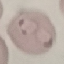 Result: malaria parasites detected. Giemsa stain. Photographed with a smartphone camera at the microscope eyepiece. Thin blood smear. Cell patch, automatically extracted from a larger field of view and resized to 64 × 64 pixels.